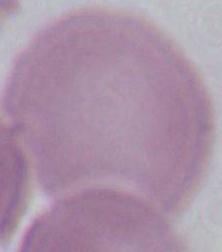

modality: photomicrograph
magnification: 1000x
identification: erythrocyte